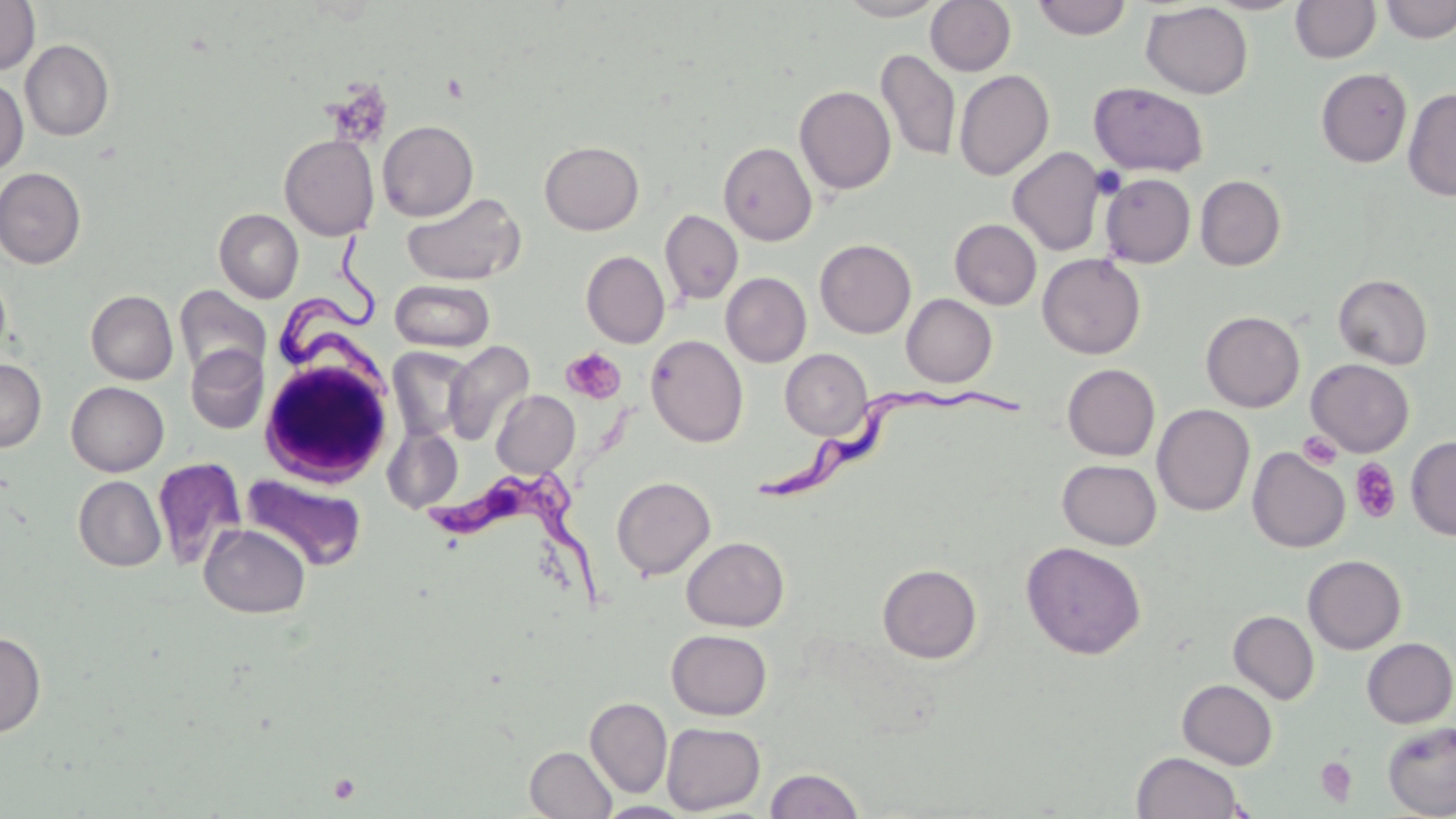
slide-level diagnosis = Trypanosoma brucei
image size = 1456×819 pixels
magnification = 1000x
field of view = single
stain = May-Grünwald-Giemsa
preparation = thin blood film
Trypanosoma brucei locations = approximate bounding boxes as (x1, y1, x2, y2) in pixels: (272, 237, 390, 389), (748, 387, 1028, 507), (428, 463, 607, 611)
uninfected red blood cell locations (subset) = approximate bounding boxes as (x1, y1, x2, y2) in pixels: (836, 0, 947, 20), (925, 0, 1016, 76), (1031, 0, 1133, 40), (1205, 0, 1305, 15), (1382, 0, 1455, 43), (0, 1, 40, 75), (1291, 1, 1380, 63), (1141, 2, 1253, 99), (20, 39, 114, 141), (876, 49, 961, 162), (1316, 68, 1412, 167), (954, 70, 1054, 180), (0, 78, 28, 175), (1090, 82, 1211, 177), (794, 85, 896, 195), (1402, 88, 1456, 201), (378, 120, 478, 221), (279, 134, 380, 240), (539, 141, 644, 235), (718, 142, 817, 246), (1007, 147, 1106, 256), (0, 167, 86, 269), (1100, 173, 1196, 268), (1195, 175, 1286, 271), (401, 191, 526, 286), (214, 209, 304, 303), (660, 210, 743, 305), (950, 219, 1041, 309), (815, 239, 916, 338), (581, 250, 670, 348), (1037, 253, 1146, 359), (721, 272, 812, 367), (1333, 273, 1433, 369), (390, 279, 494, 352), (174, 285, 270, 380), (85, 290, 178, 384), (901, 294, 997, 387), (1201, 310, 1305, 412), (645, 334, 748, 447), (443, 340, 535, 446), (186, 345, 268, 434), (387, 347, 474, 441), (780, 348, 873, 440), (0, 358, 46, 452), (1306, 359, 1414, 457), (1062, 364, 1160, 460), (66, 382, 169, 476), (491, 390, 580, 477), (1152, 404, 1255, 516), (383, 425, 463, 513), (1406, 435, 1456, 541), (1247, 447, 1350, 553), (152, 457, 246, 569), (1057, 459, 1162, 550), (241, 473, 367, 572), (74, 476, 166, 572), (611, 476, 715, 580), (199, 523, 310, 618), (681, 536, 789, 631), (1021, 541, 1146, 660), (1303, 554, 1406, 654), (877, 563, 982, 663), (1228, 610, 1319, 704), (666, 629, 772, 720), (0, 631, 46, 737), (1361, 637, 1456, 728), (1177, 679, 1277, 770), (585, 696, 672, 798), (1382, 721, 1456, 819), (661, 722, 765, 814), (525, 746, 617, 819), (1131, 751, 1246, 819), (765, 768, 864, 819), (597, 802, 693, 818)
platelet locations = approximate bounding boxes as (x1, y1, x2, y2) in pixels: (561, 348, 626, 404), (1299, 432, 1342, 470), (1349, 458, 1402, 524), (1314, 757, 1358, 807)
modality = light microscopy